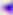

400x magnification. Toxoplasma gondii is shown. Micrograph.